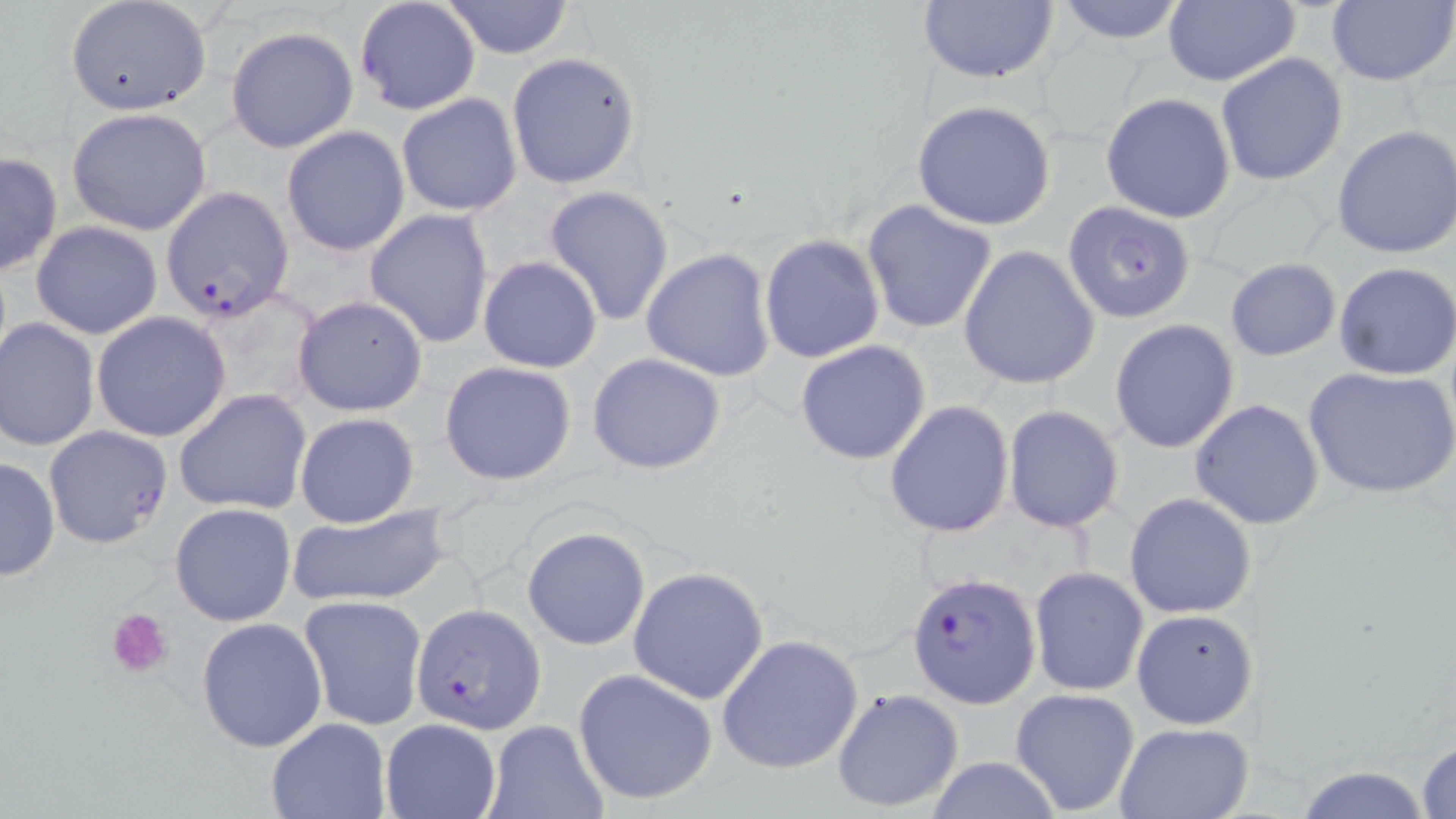
slide-level diagnosis = Plasmodium falciparum
uninfected red blood cell locations = approximate bounding boxes as (x1, y1, x2, y2) in pixels: (64, 0, 212, 119), (918, 0, 1062, 85), (1050, 0, 1190, 44), (1162, 0, 1299, 86), (1328, 0, 1456, 86), (442, 1, 575, 58), (226, 26, 361, 153), (506, 52, 642, 189), (1215, 52, 1348, 187), (397, 93, 523, 216), (1101, 93, 1236, 224), (912, 100, 1058, 230), (67, 107, 212, 236), (1331, 124, 1456, 260), (281, 126, 410, 256), (1, 151, 63, 277), (543, 185, 676, 327), (861, 199, 999, 334), (365, 208, 495, 347), (30, 221, 164, 338), (758, 234, 885, 363), (957, 244, 1101, 390), (641, 247, 776, 381), (478, 256, 603, 372), (1224, 258, 1341, 361), (1333, 262, 1456, 380), (291, 296, 428, 418), (91, 311, 231, 442), (0, 317, 99, 452), (1109, 320, 1239, 452), (794, 339, 933, 466), (587, 352, 726, 475), (439, 361, 579, 486), (1303, 364, 1456, 501), (173, 389, 313, 516), (1189, 399, 1325, 530), (884, 401, 1015, 538), (1002, 406, 1124, 533), (295, 411, 421, 528), (0, 455, 60, 582), (1123, 492, 1257, 618), (170, 502, 295, 627), (286, 504, 453, 610), (522, 525, 651, 651), (628, 566, 770, 705), (1028, 567, 1148, 697), (298, 596, 428, 731), (1131, 609, 1258, 730), (196, 618, 327, 755), (717, 635, 865, 775), (571, 668, 719, 807), (831, 687, 963, 814), (1010, 687, 1141, 816), (265, 718, 391, 819), (379, 718, 502, 819), (483, 720, 608, 819), (1112, 722, 1254, 819), (1414, 737, 1456, 819), (924, 757, 1063, 818), (1291, 763, 1437, 819)
preparation = thin blood film
stain = May-Grünwald-Giemsa
magnification = 1000x
Plasmodium falciparum-infected red blood cell locations = approximate bounding boxes as (x1, y1, x2, y2) in pixels: (353, 0, 481, 117), (169, 186, 301, 320), (1063, 196, 1198, 325), (44, 425, 174, 550), (906, 571, 1041, 709), (413, 603, 545, 734)
platelet locations = approximate bounding boxes as (x1, y1, x2, y2) in pixels: (107, 606, 173, 677)
field of view = one of a larger specimen
image size = 1456×819 pixels
modality = optical microscopy